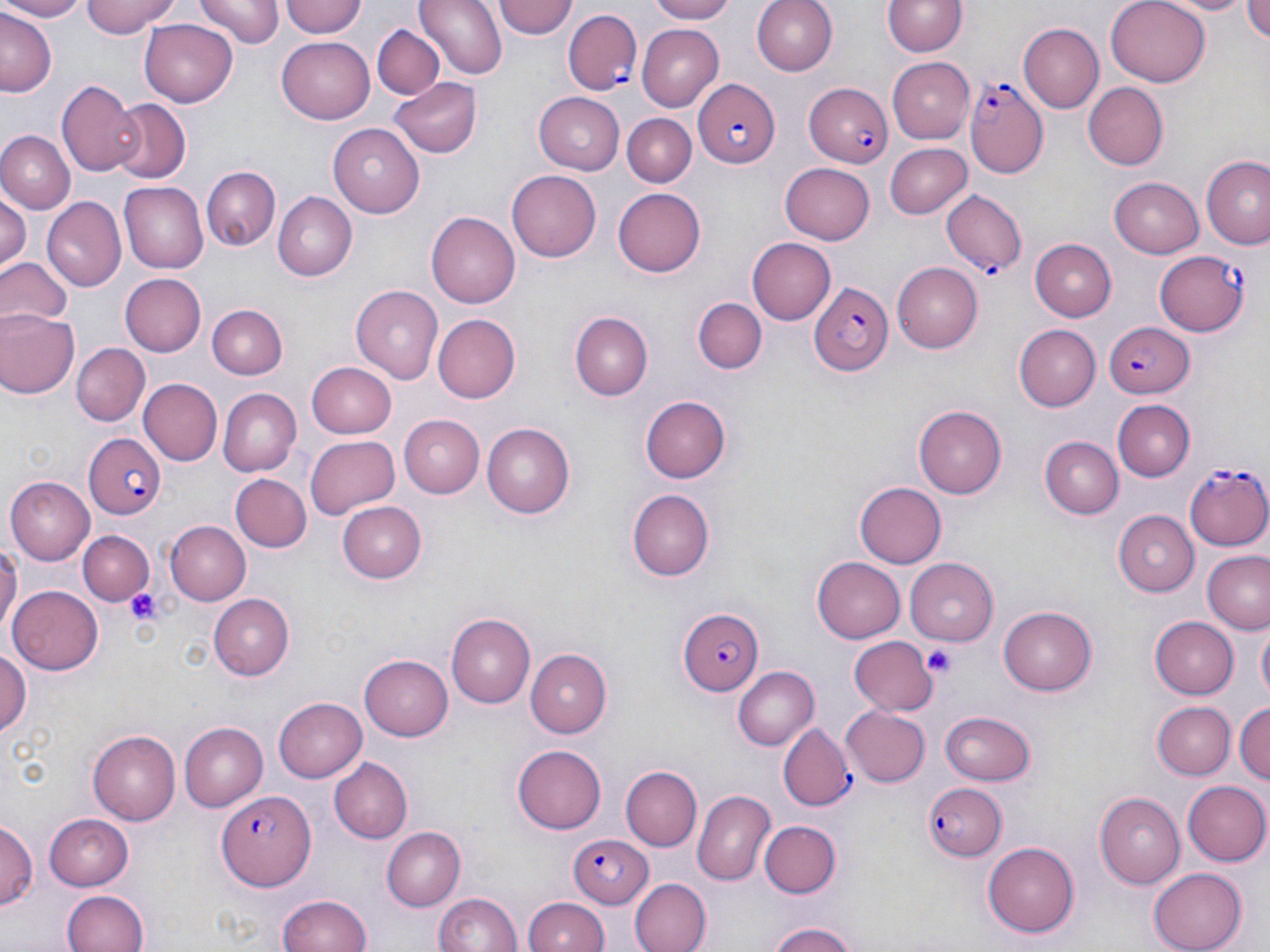

Summary:
  - Coordinate format: approximate bounding boxes as (x1, y1, x2, y2) in pixels
  - Platelet locations: (123, 587, 164, 626), (925, 645, 956, 677)
  - Uninfected red blood cell locations: (0, 0, 89, 21), (80, 0, 183, 39), (197, 0, 282, 47), (281, 0, 367, 40), (416, 0, 507, 81), (496, 0, 577, 39), (645, 0, 741, 24), (752, 0, 838, 75), (1106, 0, 1211, 86), (1167, 0, 1252, 15), (1243, 0, 1270, 47), (883, 1, 966, 57), (0, 12, 56, 95), (138, 20, 240, 108), (1019, 24, 1103, 111), (373, 25, 444, 101), (637, 25, 723, 109), (277, 33, 376, 121), (888, 57, 975, 142), (390, 78, 480, 156), (59, 82, 144, 175), (1083, 83, 1169, 170), (532, 93, 625, 174), (111, 99, 191, 185), (622, 113, 696, 187), (328, 124, 426, 215), (0, 129, 74, 211), (885, 142, 972, 218), (1201, 155, 1270, 249), (778, 162, 876, 244), (202, 166, 280, 251), (507, 169, 603, 262), (1109, 176, 1204, 258), (120, 182, 208, 272), (611, 187, 706, 277), (0, 192, 29, 268), (273, 192, 355, 281), (43, 196, 126, 292), (426, 211, 523, 307), (746, 238, 836, 326), (1028, 238, 1116, 321), (0, 258, 73, 328), (895, 261, 984, 354), (120, 273, 205, 356), (350, 285, 444, 384), (692, 294, 768, 377), (208, 303, 287, 379), (0, 310, 81, 398), (570, 312, 652, 400), (431, 313, 520, 404), (1013, 325, 1099, 410), (72, 344, 148, 426), (309, 361, 398, 436), (139, 379, 223, 466), (216, 389, 300, 478), (641, 395, 732, 482), (1111, 400, 1194, 481), (914, 405, 1006, 498), (396, 413, 484, 498), (483, 424, 574, 517), (305, 435, 398, 518), (1042, 436, 1122, 518), (231, 474, 310, 552), (6, 476, 94, 564), (853, 482, 944, 568), (627, 489, 714, 579), (335, 501, 429, 583), (1112, 511, 1198, 596), (168, 520, 251, 606), (79, 530, 152, 605), (0, 536, 19, 639), (1202, 552, 1270, 635), (812, 557, 904, 642), (904, 559, 999, 647), (8, 585, 104, 675), (209, 594, 292, 680), (999, 607, 1098, 694), (446, 613, 534, 707), (1152, 615, 1238, 698), (1259, 626, 1270, 700), (850, 637, 936, 714), (525, 647, 613, 737), (0, 648, 29, 744), (359, 652, 454, 738), (732, 666, 817, 751), (274, 696, 367, 783), (1153, 702, 1236, 780), (1234, 702, 1270, 788), (842, 705, 931, 787), (940, 710, 1038, 788), (179, 721, 266, 811), (87, 730, 180, 824), (512, 744, 607, 833), (329, 758, 413, 844), (619, 766, 701, 852), (1183, 781, 1269, 866), (694, 790, 774, 885), (1094, 792, 1184, 889), (42, 812, 136, 890), (0, 819, 37, 915), (758, 820, 840, 898), (380, 827, 464, 911), (981, 843, 1082, 938), (1150, 865, 1247, 950), (630, 878, 710, 952), (60, 890, 147, 952), (277, 892, 374, 952), (434, 892, 524, 952), (523, 895, 609, 952), (764, 920, 866, 952)
  - Plasmodium falciparum-infected red blood cell locations: (564, 9, 643, 96), (691, 79, 781, 168), (965, 83, 1049, 177), (803, 84, 895, 167), (942, 192, 1027, 274), (1154, 249, 1250, 336), (807, 282, 893, 377), (1105, 320, 1192, 399), (81, 431, 165, 519), (1184, 462, 1270, 550), (676, 605, 765, 696), (778, 725, 854, 811), (922, 781, 1007, 862), (214, 789, 314, 890), (565, 835, 655, 907)
  - Slide-level diagnosis: Plasmodium falciparum
  - Modality: light microscopy
  - Magnification: 1000x
  - Stain: May-Grünwald-Giemsa
  - Preparation: thin blood smear
  - Image size: 1270×952 pixels
  - Field of view: one of a larger specimen